Assess this cell for malaria.
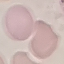

Uninfected.

Summary:
  - Image type: cell patch, automatically extracted from a larger field of view and resized to 64 × 64 pixels
  - Capture: smartphone camera at the microscope eyepiece
  - Stain: Giemsa
  - Preparation: thin blood film